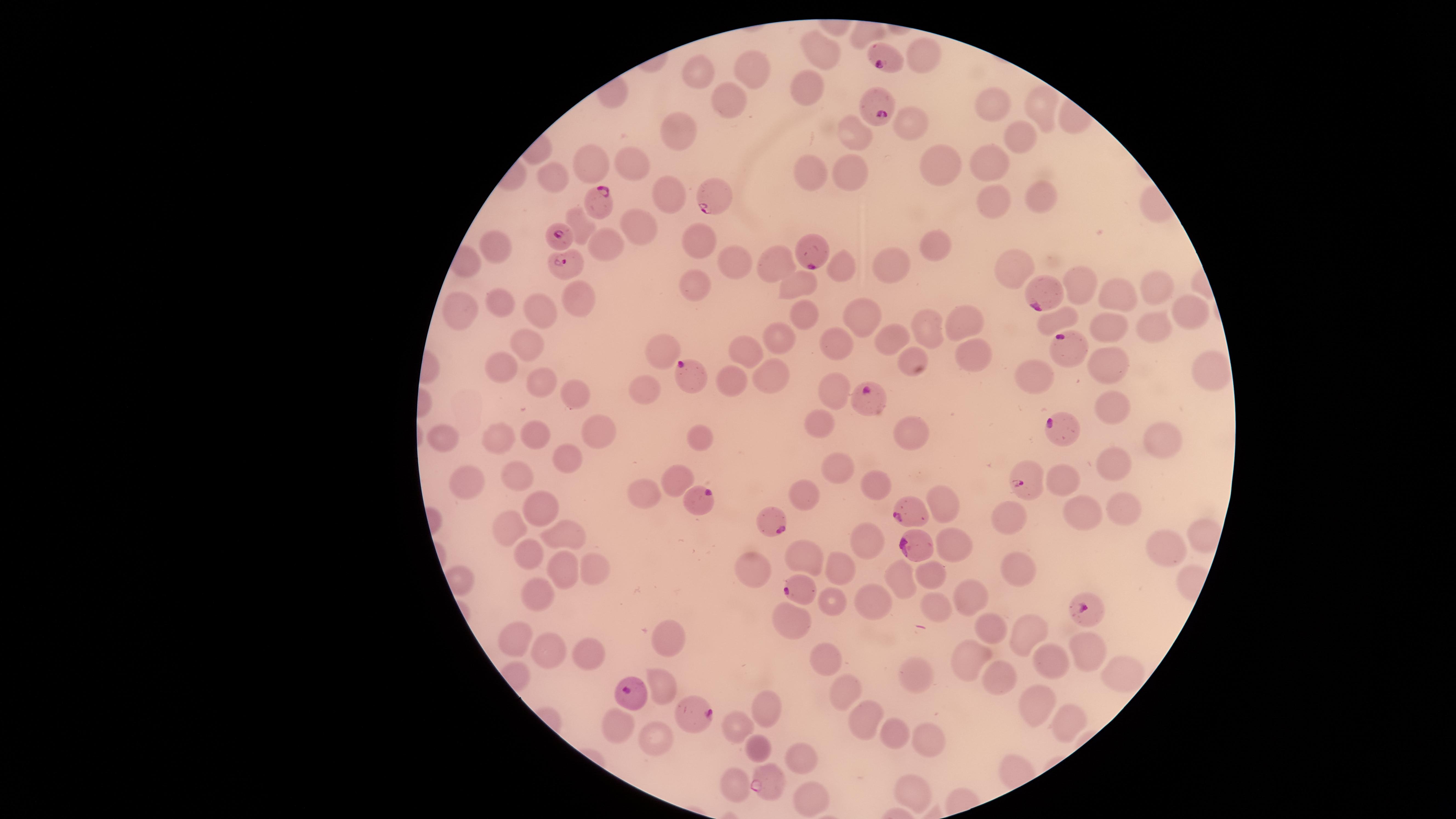

Approximate marker points as [x, y] in pixels.
Summary:
  - Uninfected RBCs: [921, 50], [823, 51], [752, 66], [694, 67], [807, 85], [728, 96], [994, 100], [1043, 103], [909, 122], [680, 125], [1019, 130], [858, 134], [590, 157], [994, 157], [628, 160], [931, 162], [848, 168], [808, 172], [546, 179], [667, 188], [1040, 193], [999, 205], [638, 223], [700, 236], [612, 242], [492, 243], [933, 243], [775, 259], [889, 260], [730, 261], [842, 263], [1010, 271], [803, 279], [1084, 282], [701, 286], [1159, 287], [1122, 294], [579, 298], [493, 299], [458, 304], [531, 309], [805, 310], [859, 313], [1199, 315], [1060, 319], [965, 321], [1145, 326], [1108, 327], [930, 330], [773, 334], [892, 337], [532, 340], [840, 340], [745, 349], [660, 350], [914, 355], [978, 356], [1112, 363], [1210, 363], [506, 370], [1038, 373], [769, 378], [544, 381], [737, 384], [837, 386], [647, 387], [574, 392], [1112, 406], [818, 424], [596, 430], [912, 430], [493, 433], [531, 433], [446, 435], [696, 438], [1157, 439], [572, 456], [1115, 459], [836, 465], [517, 475], [1069, 475], [472, 477], [674, 479], [877, 481], [801, 491], [639, 495], [947, 498], [536, 506], [1121, 507], [1077, 511], [1011, 515], [507, 530], [562, 534], [865, 534], [1200, 534], [952, 541], [1161, 541], [527, 554], [809, 554], [753, 562], [593, 563], [838, 568], [562, 569], [925, 572], [1021, 573], [902, 576], [961, 588], [544, 594], [871, 598], [837, 601], [934, 602], [788, 614], [990, 627], [1027, 629], [668, 640], [516, 646], [583, 649], [552, 650], [1088, 650], [826, 651], [970, 659], [1054, 662], [1117, 670], [911, 673], [1004, 677], [664, 682], [846, 690], [1041, 699], [764, 707], [1057, 716], [863, 718], [737, 725], [625, 729], [894, 733], [657, 735], [926, 737], [757, 748], [799, 756], [732, 779], [917, 789], [804, 793]
  - Parasitized RBCs: [882, 59], [878, 109], [709, 199], [600, 204], [562, 236], [811, 253], [562, 263], [1040, 293], [1069, 344], [693, 375], [868, 397], [1064, 426], [1022, 484], [697, 501], [911, 515], [775, 516], [912, 548], [800, 593], [1085, 606], [631, 695], [700, 712], [764, 778]
  - Species: Plasmodium falciparum
  - Capture: smartphone photograph through the microscope eyepiece
  - Presence: malaria parasites detected
  - Preparation: thin smear of blood
  - Stain: Giemsa
  - Field of view: single
  - Image size: 1456×819 pixels
  - Visible region: circular